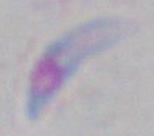

Summary:
  - Magnification: 1000x
  - Identification: Toxoplasma gondii
  - Modality: micrograph